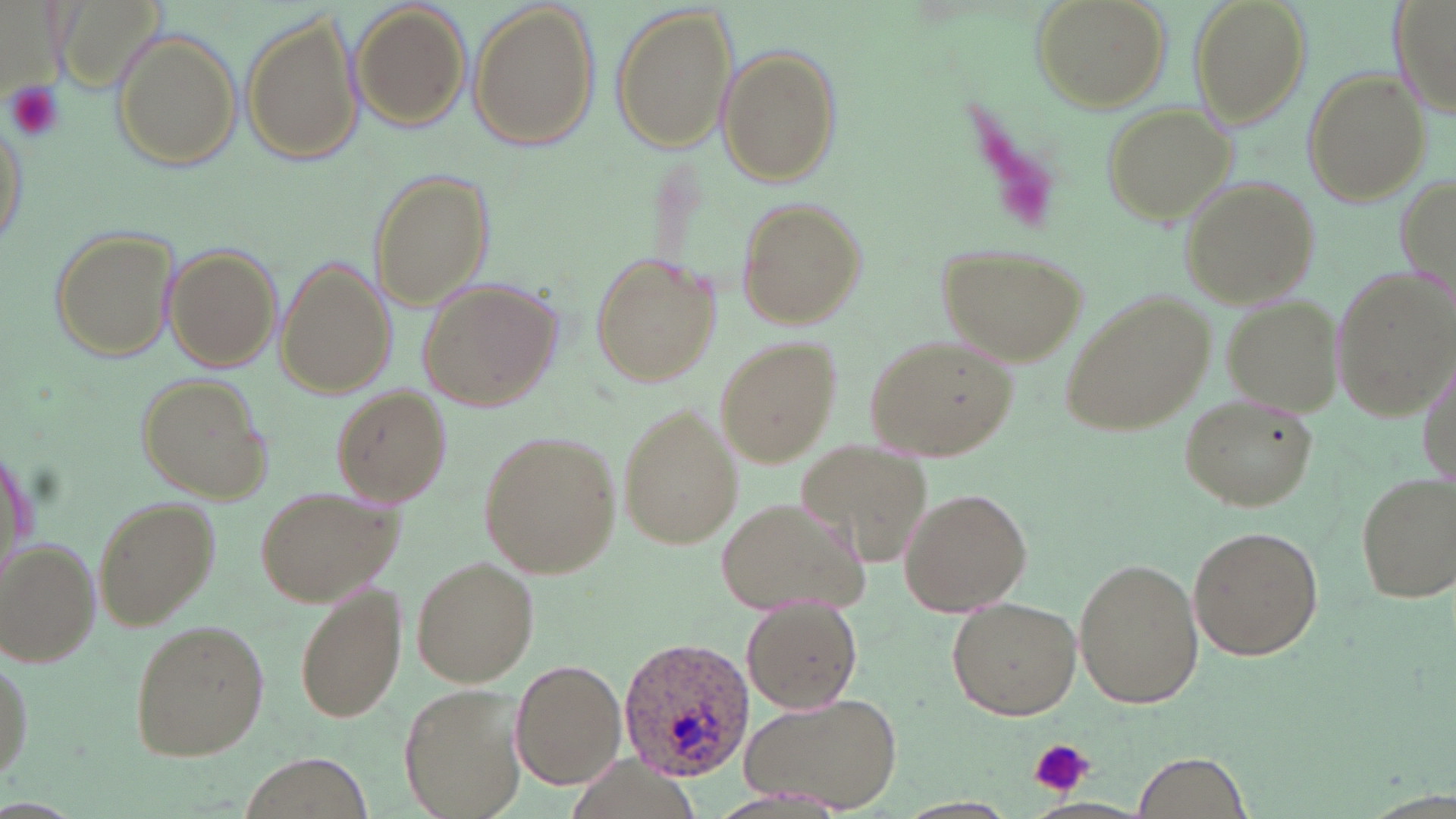
slide-level diagnosis = Plasmodium ovale
magnification = 1000x
uninfected red blood cell locations = approximate bounding boxes as [x1, y1, x2, y2] in pixels: [1033, 0, 1171, 113], [1191, 0, 1310, 130], [1390, 0, 1456, 120], [50, 3, 170, 98], [471, 4, 598, 152], [612, 4, 738, 154], [350, 5, 469, 132], [241, 14, 364, 167], [111, 30, 241, 171], [718, 47, 841, 185], [1302, 70, 1428, 206], [1105, 104, 1239, 224], [0, 111, 29, 251], [368, 169, 493, 310], [1180, 177, 1319, 309], [737, 201, 866, 329], [48, 225, 180, 363], [165, 244, 283, 371], [940, 245, 1086, 365], [589, 251, 722, 389], [278, 256, 394, 400], [1330, 264, 1455, 422], [418, 279, 561, 411], [1064, 291, 1215, 436], [1223, 296, 1346, 417], [863, 334, 1020, 463], [714, 339, 840, 468], [135, 371, 272, 504], [331, 387, 449, 507], [1178, 392, 1318, 513], [615, 402, 744, 553], [480, 430, 621, 576], [1, 436, 37, 589], [799, 440, 938, 568], [1356, 470, 1455, 604], [256, 483, 403, 606], [897, 487, 1033, 615], [91, 494, 221, 629], [714, 495, 869, 615], [1188, 525, 1322, 660], [2, 540, 100, 667], [409, 554, 540, 688], [1072, 556, 1204, 709], [296, 581, 405, 725], [944, 597, 1081, 720], [744, 601, 862, 714], [126, 621, 269, 763], [0, 643, 35, 788], [509, 657, 627, 789], [398, 682, 528, 816], [739, 691, 903, 812], [1132, 751, 1250, 817]
modality = light microscopy
platelet locations = approximate bounding boxes as [x1, y1, x2, y2] in pixels: [4, 81, 65, 143], [1030, 738, 1093, 797]
preparation = thin blood film
stain = May-Grünwald-Giemsa
field of view = single
Plasmodium ovale-infected red blood cell locations = approximate bounding boxes as [x1, y1, x2, y2] in pixels: [611, 637, 755, 782]
image size = 1456×819 pixels